Locate every Plasmodium ovale-infected red blood cell.
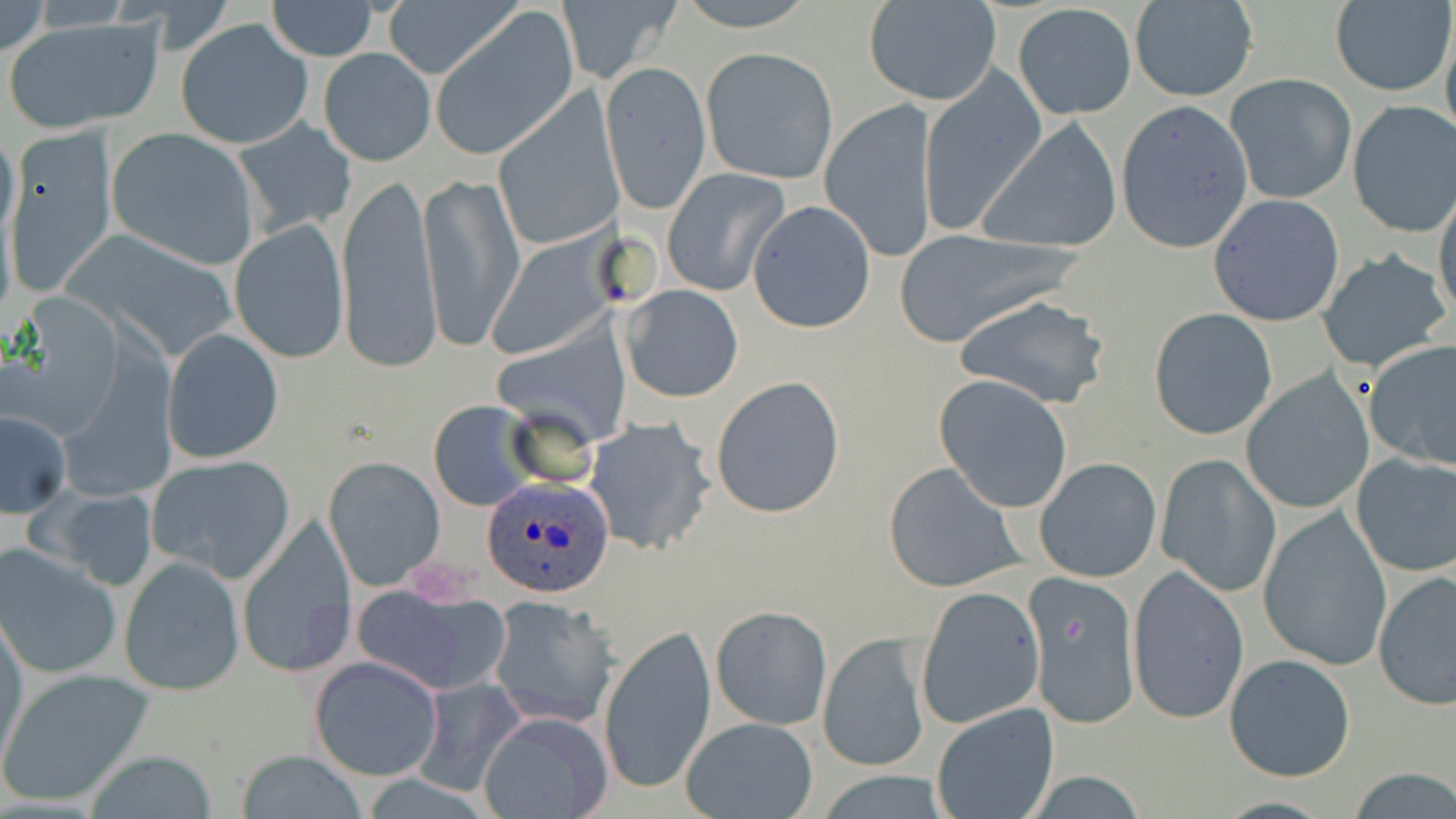
Approximate bounding boxes as [x1, y1, x2, y2] in pixels.
Plasmodium ovale-infected red blood cells: [481, 476, 617, 599].

Uninfected red blood cell locations: [0, 0, 49, 60], [673, 0, 820, 30], [266, 1, 380, 60], [383, 1, 517, 81], [557, 1, 683, 85], [863, 1, 1002, 107], [1331, 2, 1454, 97], [1014, 3, 1137, 121], [1127, 3, 1257, 102], [431, 10, 578, 160], [4, 17, 164, 133], [177, 18, 313, 150], [319, 47, 436, 166], [701, 47, 839, 185], [599, 61, 712, 214], [919, 69, 1046, 235], [1226, 74, 1356, 204], [492, 96, 623, 251], [820, 98, 939, 259], [1114, 100, 1254, 255], [1348, 102, 1456, 237], [235, 116, 357, 237], [976, 119, 1121, 255], [6, 125, 117, 294], [106, 128, 260, 270], [662, 168, 789, 298], [419, 169, 523, 354], [338, 170, 443, 375], [1434, 189, 1456, 325], [1208, 192, 1346, 327], [747, 200, 876, 333], [229, 219, 348, 363], [889, 227, 1083, 347], [488, 229, 620, 362], [1317, 250, 1452, 372], [620, 284, 745, 403], [956, 293, 1110, 408], [1148, 308, 1277, 439], [162, 327, 284, 463], [1363, 339, 1456, 471], [1242, 373, 1373, 514], [710, 375, 845, 519], [934, 375, 1075, 514], [429, 401, 536, 512], [1, 411, 71, 517], [583, 417, 716, 558], [1350, 453, 1456, 576], [1157, 454, 1281, 597], [146, 456, 295, 583], [325, 456, 446, 590], [1035, 457, 1162, 582], [883, 462, 1024, 594], [37, 487, 160, 588], [1257, 508, 1393, 671], [234, 516, 358, 679], [0, 545, 124, 681], [119, 556, 244, 697], [1127, 566, 1250, 726], [1373, 570, 1456, 709], [1023, 574, 1143, 730], [350, 580, 510, 696], [915, 585, 1044, 729], [488, 597, 616, 730], [710, 605, 833, 730], [0, 613, 28, 767], [599, 623, 717, 798], [818, 631, 933, 773], [1225, 654, 1355, 782], [308, 656, 442, 780], [0, 668, 152, 807], [414, 676, 524, 794], [929, 703, 1058, 817], [477, 712, 612, 819], [681, 717, 819, 819], [238, 749, 367, 818], [87, 750, 218, 818], [1347, 768, 1456, 818], [808, 771, 951, 819]. Slide-level diagnosis: Plasmodium ovale. Optical microscopy. May-Grünwald-Giemsa stain. Thin blood smear. One field of a larger specimen. Image is 1456×819 pixels. 1000x magnification.